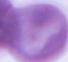
magnification: 1000x
modality: photomicrograph
identification: erythrocyte